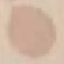

Summary:
  - Result: no malaria parasites detected
  - Image type: cell patch, automatically extracted from a larger field of view and resized to 64 × 64 pixels
  - Capture: smartphone camera at the microscope eyepiece
  - Stain: Giemsa
  - Preparation: thin smear